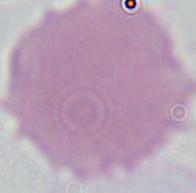

Captured at 1000x magnification. Micrograph. An erythrocyte is shown.